Report the malaria status.
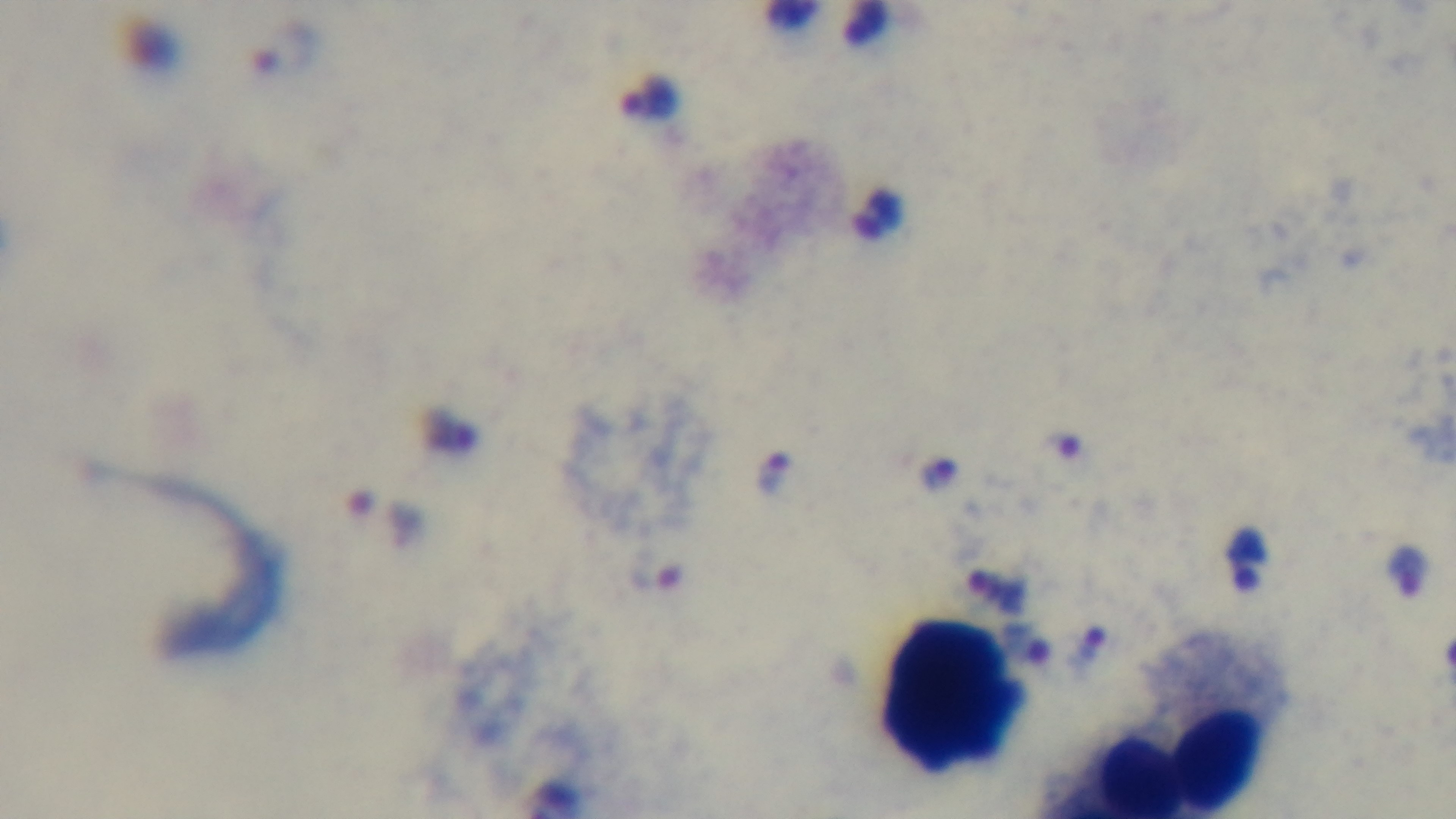
It is infected.

Photomicrograph. Mounted 4K digital camera. Preparation: thick. Single field of view. Giemsa stain. Oil-immersion objective, 100x.